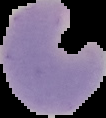
preparation = thin blood smear
image size = 106×118 pixels
image type = segmented cell region on a black background
malaria status = parasitized